Report the malaria status of this cell.
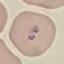

It is parasitized.

capture = smartphone camera at the microscope eyepiece
stain = Giemsa
preparation = thin smear
image type = cell patch, automatically extracted from a larger field of view and resized to 64 × 64 pixels